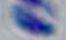
Summary:
  - Magnification: 1000x
  - Modality: micrograph
  - Identification: Toxoplasma gondii